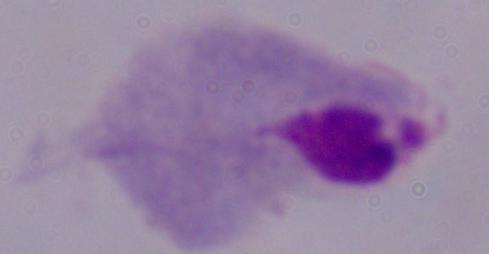

identification = trichomonad
modality = photomicrograph
magnification = 1000x